Identify the parasite.
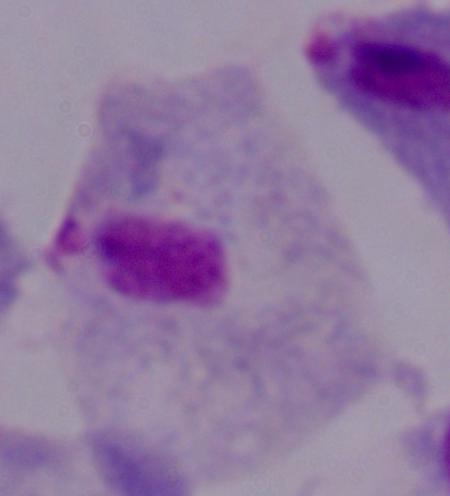

This is a trichomonad.

Captured at 1000x magnification. Photomicrograph.